Comment on the morphology of the erythrocytes.
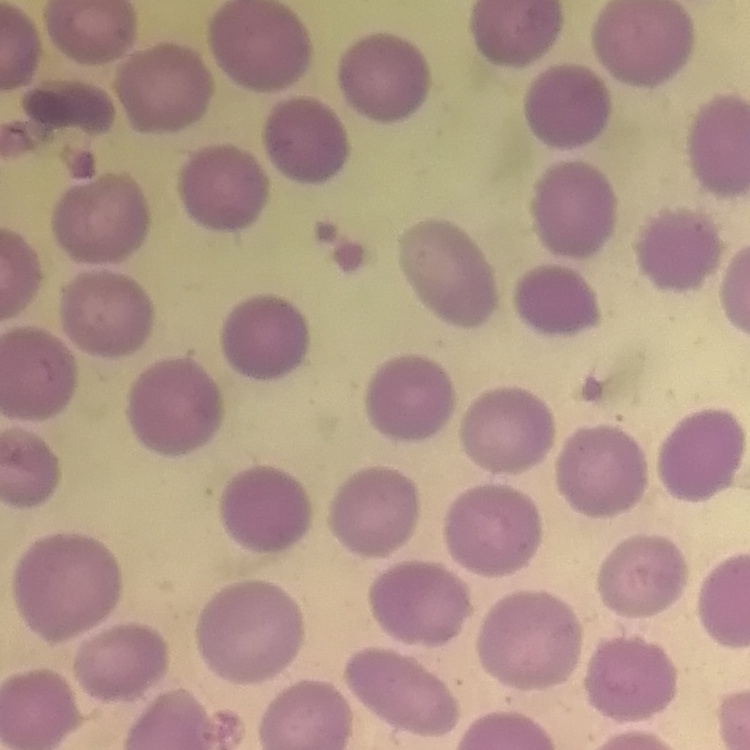
They show no rouleaux formation.

stain = Field's or Giemsa
image type = square crop of a larger photomicrograph
preparation = thin blood smear